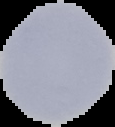
Summary:
  - Image type: segmented cell region with the area outside set to black
  - Image size: 115×127 pixels
  - Result: negative for Plasmodium parasites
  - Preparation: thin blood smear